Locate every malaria parasite.
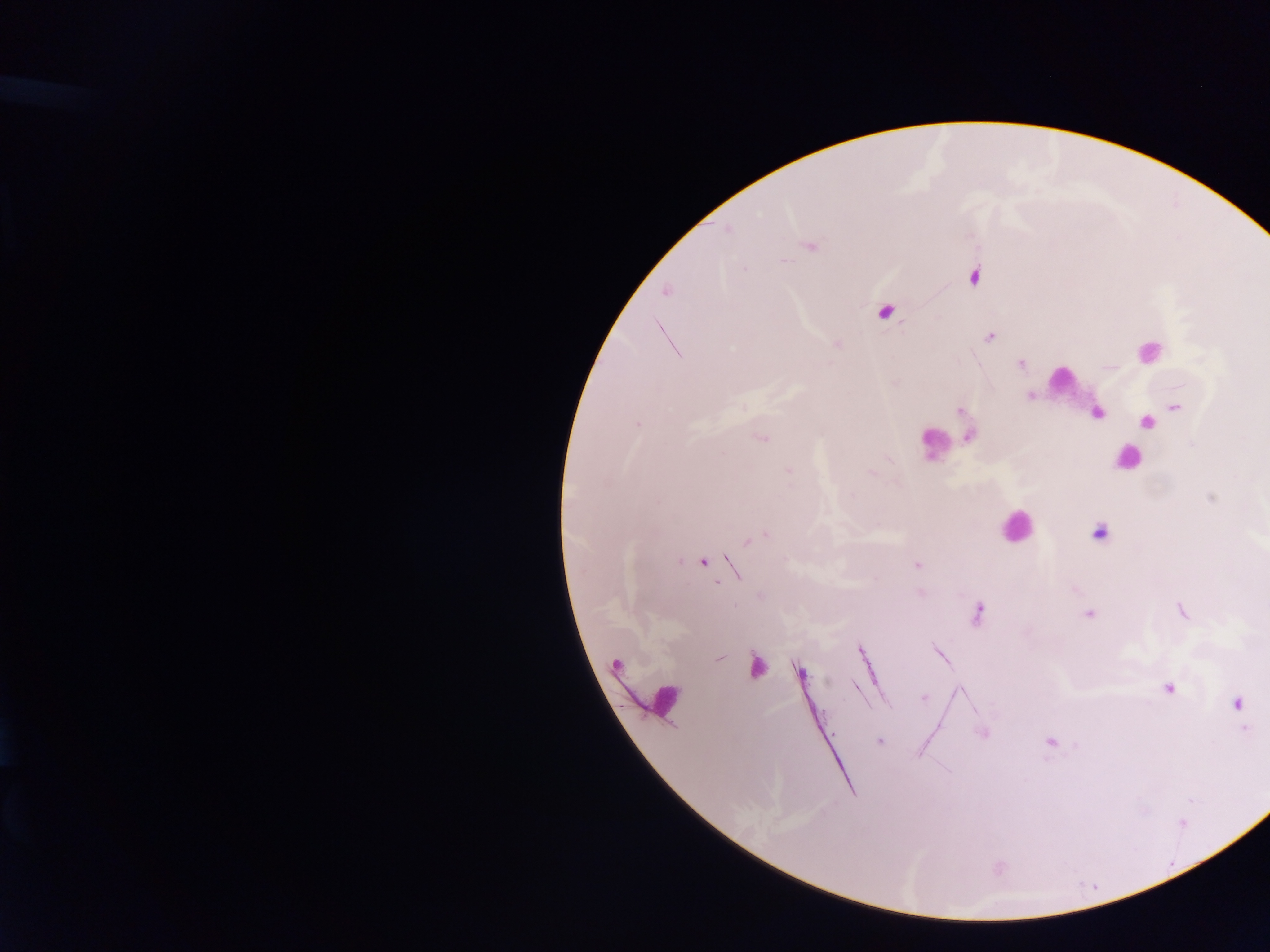
Approximate centers as (x, y) in pixels.
Malaria parasites: (812, 246), (783, 261), (974, 275), (664, 292), (884, 312), (990, 336), (837, 345), (1018, 363), (1177, 408), (959, 410), (1099, 412), (1147, 422), (968, 437), (760, 438), (789, 471), (871, 472), (1210, 498), (1098, 531), (703, 562), (916, 565), (920, 592), (1181, 611), (978, 612), (1089, 613), (756, 666), (800, 673), (816, 678), (826, 681), (1169, 687), (925, 700), (1236, 702), (982, 734), (878, 741), (1049, 742).

Leukocyte locations: (1146, 352), (1065, 383), (1129, 460), (1014, 530). Image is 1270×952 pixels. Mobile-phone photograph taken through the microscope. Collected in Ghana. Thick blood film. Single field of view.